Assess this cell for malaria.
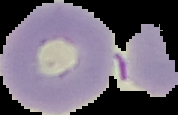
It is uninfected.

Cell region segmented out of the field of view; the surrounding area is masked to black. From a thin blood smear. Image is 178×115 pixels.